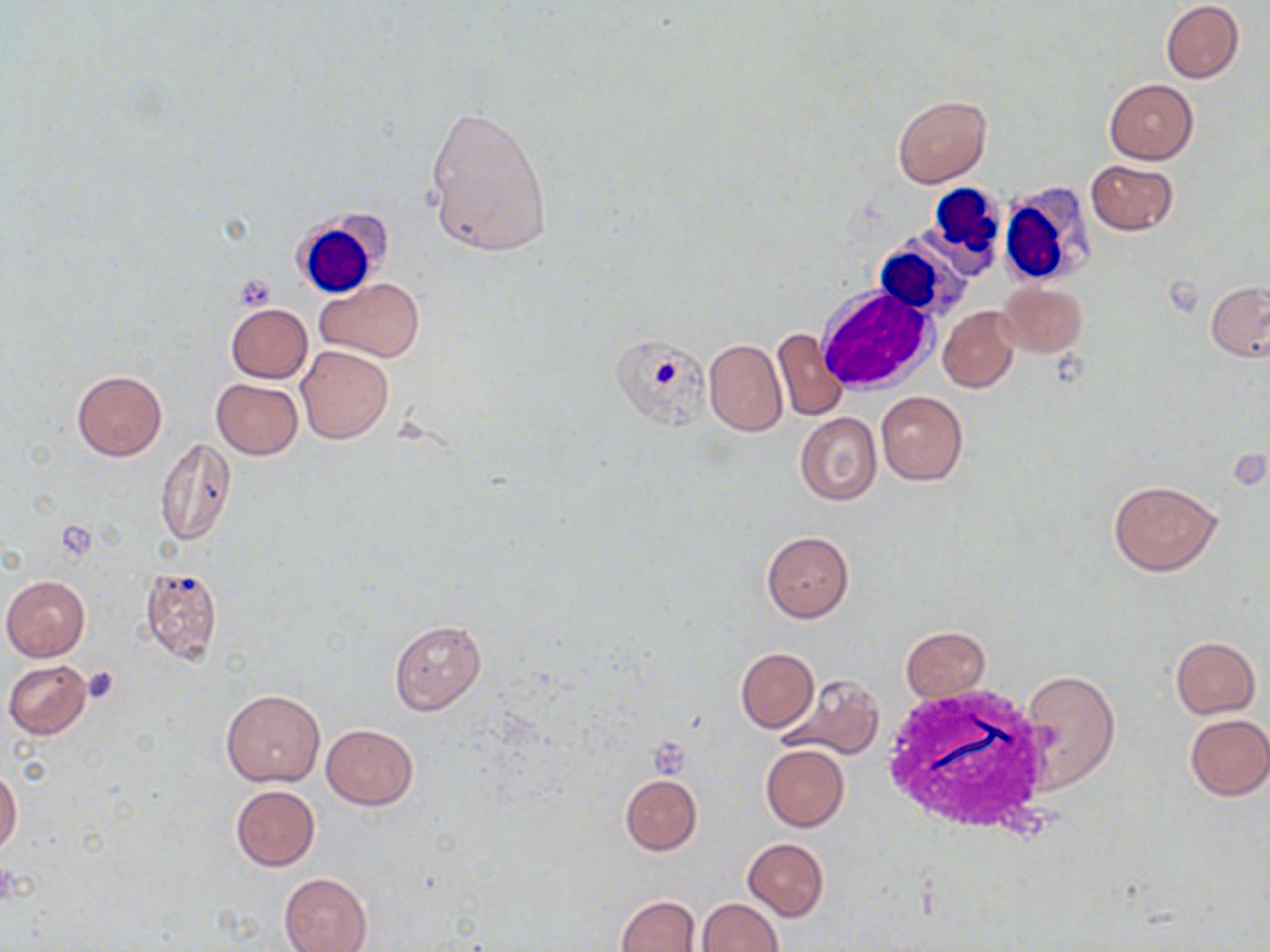 Approximate bounding boxes as named x1/y1/x2/y2 corners in pixels. Uninfected red blood cell locations: (x1=1161, y1=1, x2=1244, y2=84), (x1=1104, y1=79, x2=1199, y2=164), (x1=891, y1=94, x2=991, y2=187), (x1=423, y1=103, x2=552, y2=259), (x1=1085, y1=159, x2=1178, y2=235), (x1=316, y1=278, x2=424, y2=361), (x1=1206, y1=280, x2=1270, y2=361), (x1=997, y1=283, x2=1089, y2=357), (x1=225, y1=304, x2=313, y2=383), (x1=937, y1=306, x2=1019, y2=392), (x1=772, y1=327, x2=850, y2=422), (x1=704, y1=338, x2=787, y2=437), (x1=296, y1=345, x2=394, y2=444), (x1=72, y1=370, x2=167, y2=461), (x1=211, y1=378, x2=303, y2=459), (x1=875, y1=391, x2=969, y2=486), (x1=795, y1=413, x2=881, y2=505), (x1=154, y1=439, x2=236, y2=548), (x1=1107, y1=479, x2=1222, y2=576), (x1=762, y1=531, x2=853, y2=622), (x1=138, y1=565, x2=224, y2=665), (x1=1, y1=575, x2=91, y2=661), (x1=389, y1=620, x2=486, y2=713), (x1=901, y1=627, x2=991, y2=701), (x1=1170, y1=635, x2=1260, y2=718), (x1=734, y1=648, x2=818, y2=733), (x1=3, y1=658, x2=93, y2=739), (x1=1020, y1=670, x2=1120, y2=790), (x1=777, y1=673, x2=884, y2=760), (x1=221, y1=689, x2=325, y2=788), (x1=1182, y1=714, x2=1270, y2=801), (x1=321, y1=724, x2=418, y2=810), (x1=761, y1=744, x2=849, y2=832), (x1=0, y1=765, x2=22, y2=856), (x1=619, y1=774, x2=702, y2=855), (x1=230, y1=786, x2=319, y2=871), (x1=742, y1=838, x2=828, y2=920), (x1=279, y1=872, x2=372, y2=952), (x1=613, y1=894, x2=702, y2=952), (x1=695, y1=899, x2=783, y2=951). White blood cell locations: (x1=998, y1=175, x2=1107, y2=283), (x1=923, y1=183, x2=1007, y2=276), (x1=291, y1=211, x2=386, y2=299), (x1=876, y1=238, x2=971, y2=326), (x1=817, y1=286, x2=936, y2=394), (x1=881, y1=684, x2=1061, y2=837). Platelet locations: (x1=234, y1=273, x2=277, y2=310), (x1=80, y1=666, x2=122, y2=705), (x1=649, y1=737, x2=691, y2=778), (x1=0, y1=858, x2=17, y2=908). Slide-level diagnosis: negative for blood parasites. May-Grünwald-Giemsa stain. One field of a larger specimen. Image is 1270×952 pixels. Captured at 1000x magnification. Thin blood smear. Light microscopy.